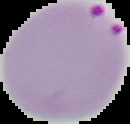
Summary:
  - Image size: 130×124 pixels
  - Preparation: thin blood film
  - Image type: segmented cell region on a black background
  - Malaria status: parasitized